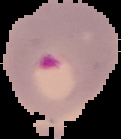

preparation: thin blood film
image_size: 121×139 pixels
image_type: segmented cell region on a black background
result: Plasmodium parasites detected